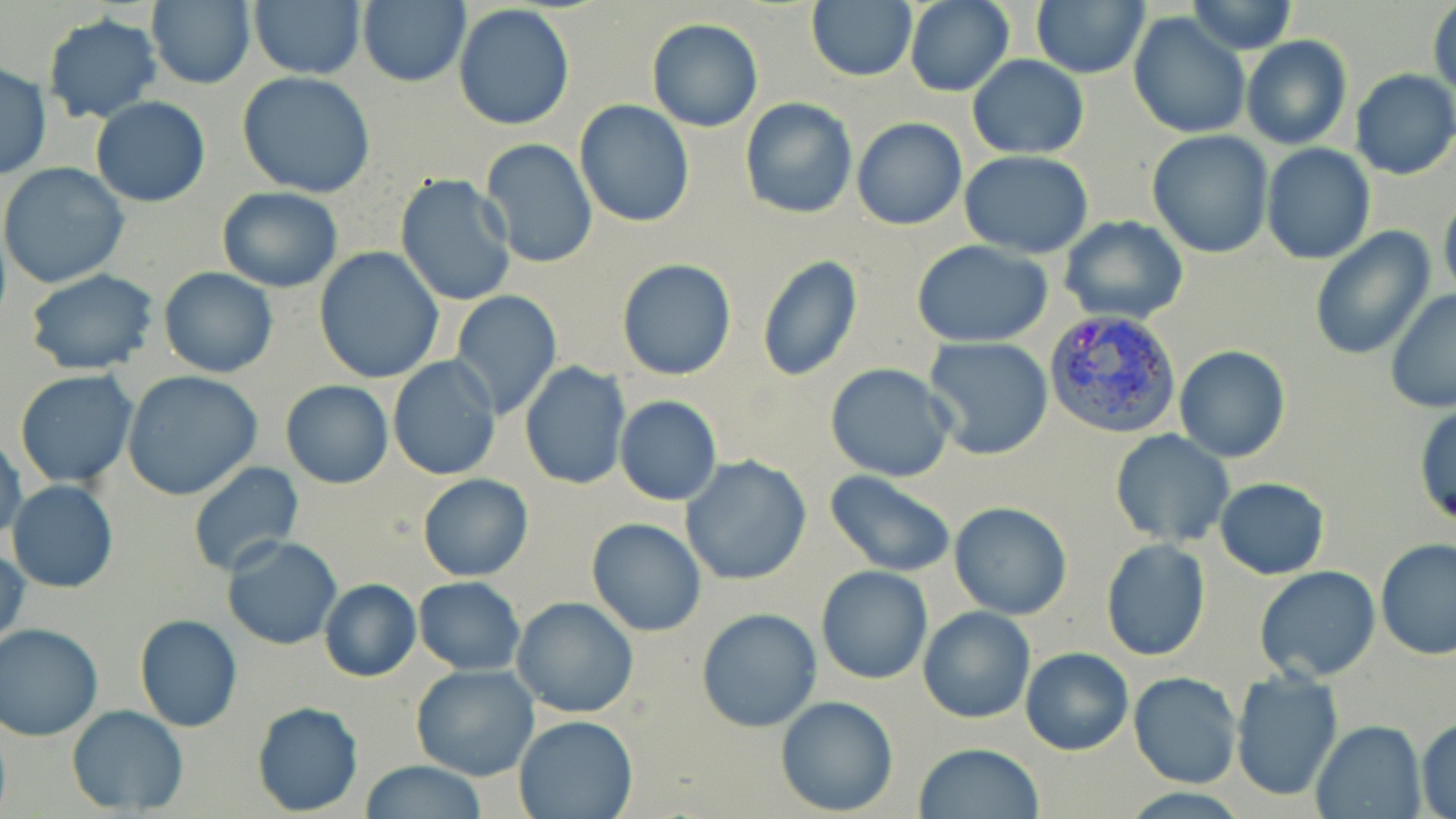

slide-level diagnosis = Plasmodium vivax
uninfected red blood cell locations = approximate bounding boxes as (x1,y1)-(x2,y2) corner pairs in pixels: (357,0)-(470,87), (806,0)-(918,82), (905,0)-(1013,96), (1030,0)-(1149,79), (144,1)-(255,88), (1185,1)-(1298,54), (247,2)-(366,79), (1430,2)-(1456,101), (453,5)-(574,131), (1128,11)-(1251,139), (43,14)-(162,123), (648,18)-(763,132), (1241,35)-(1353,150), (967,55)-(1089,159), (0,64)-(51,179), (1351,69)-(1456,180), (237,72)-(376,198), (90,95)-(211,207), (738,98)-(857,219), (575,101)-(694,228), (851,118)-(967,231), (1147,131)-(1274,259), (480,139)-(599,269), (1261,145)-(1375,264), (959,152)-(1096,256), (0,162)-(130,288), (395,174)-(520,307), (217,186)-(343,292), (1439,192)-(1456,303), (1059,216)-(1189,326), (1309,228)-(1435,359), (911,240)-(1055,348), (314,248)-(443,383), (755,253)-(861,383), (616,258)-(737,381), (158,267)-(278,378), (24,270)-(160,375), (1385,288)-(1456,413), (448,291)-(563,421), (922,337)-(1054,460), (1174,345)-(1291,462), (387,358)-(501,481), (519,361)-(631,488), (826,363)-(956,483), (13,369)-(139,489), (122,371)-(261,500), (281,380)-(394,488), (615,395)-(722,505), (1412,401)-(1455,529), (1109,430)-(1233,547), (0,432)-(25,547), (681,456)-(811,587), (188,460)-(305,579), (824,472)-(958,578), (417,473)-(534,582), (1214,478)-(1329,579), (7,480)-(119,594), (949,501)-(1073,620), (587,518)-(707,637), (222,536)-(343,651), (1100,539)-(1210,661), (1374,539)-(1456,659), (1,545)-(28,656), (814,565)-(933,686), (1255,565)-(1382,681), (413,576)-(525,674), (318,578)-(421,682), (512,596)-(639,719), (917,605)-(1035,724), (695,607)-(823,733), (135,614)-(241,732), (0,623)-(103,742), (1020,647)-(1134,755), (411,665)-(540,781), (1228,668)-(1343,802), (1129,673)-(1244,788), (774,695)-(899,817), (252,701)-(364,816), (67,705)-(188,815), (513,714)-(638,819), (1416,716)-(1455,819), (1312,719)-(1425,819), (913,743)-(1045,819), (359,760)-(487,818)
image size = 1456×819 pixels
stain = May-Grünwald-Giemsa
modality = light microscopy
preparation = thin blood film
field of view = one of a larger specimen
magnification = 1000x
Plasmodium vivax-infected red blood cell locations = approximate bounding boxes as (x1,y1)-(x2,y2) corner pairs in pixels: (1044,308)-(1183,440)